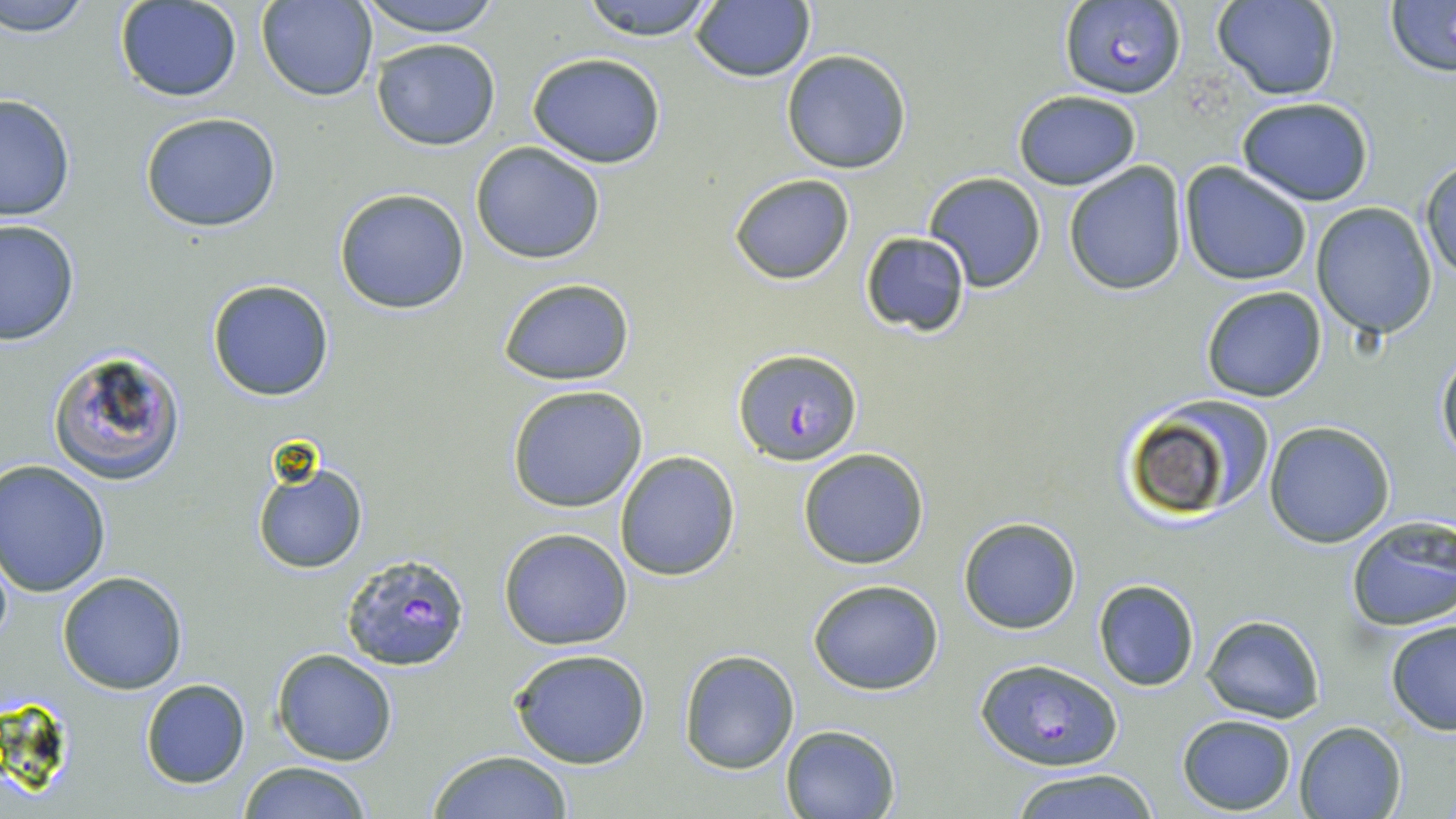

Plasmodium falciparum-infected red blood cell locations = approximate bounding boxes as (x1, y1, x2, y2) in pixels: (1058, 2, 1187, 101), (733, 345, 861, 464), (339, 553, 472, 672), (977, 658, 1120, 770)
slide-level diagnosis = Plasmodium falciparum
stain = May-Grünwald-Giemsa
uninfected red blood cell locations = approximate bounding boxes as (x1, y1, x2, y2) in pixels: (2, 0, 94, 38), (351, 0, 507, 37), (577, 0, 722, 40), (1212, 0, 1341, 101), (1385, 0, 1456, 75), (256, 1, 378, 103), (115, 2, 243, 103), (689, 3, 816, 83), (371, 38, 502, 152), (780, 50, 912, 174), (527, 52, 667, 169), (1011, 90, 1141, 190), (0, 94, 75, 223), (1235, 97, 1375, 205), (138, 111, 283, 232), (470, 142, 605, 265), (1419, 159, 1455, 282), (1062, 161, 1187, 296), (1180, 162, 1313, 285), (727, 172, 856, 284), (923, 172, 1046, 293), (334, 188, 471, 314), (1310, 202, 1437, 340), (0, 219, 79, 346), (860, 232, 971, 337), (207, 278, 334, 401), (497, 278, 636, 387), (1200, 286, 1328, 402), (46, 346, 187, 486), (1436, 347, 1456, 465), (506, 384, 649, 513), (1113, 396, 1271, 526), (1264, 420, 1394, 547), (797, 447, 929, 570), (614, 451, 740, 581), (250, 452, 370, 576), (2, 458, 113, 597), (957, 516, 1082, 634), (1344, 518, 1456, 631), (498, 528, 633, 649), (57, 571, 189, 694), (807, 579, 945, 695), (1092, 579, 1202, 692), (1202, 615, 1324, 722), (1385, 617, 1456, 737), (271, 647, 399, 767), (510, 647, 654, 769), (679, 649, 799, 774), (138, 679, 251, 788), (1176, 714, 1297, 814), (1294, 720, 1406, 819), (781, 725, 900, 818), (427, 749, 575, 819), (236, 761, 373, 819), (1001, 769, 1163, 819)
magnification = 1000x
modality = light microscopy
field of view = one of a larger specimen
preparation = thin blood smear
image size = 1456×819 pixels